Describe the morphology of the erythrocytes.
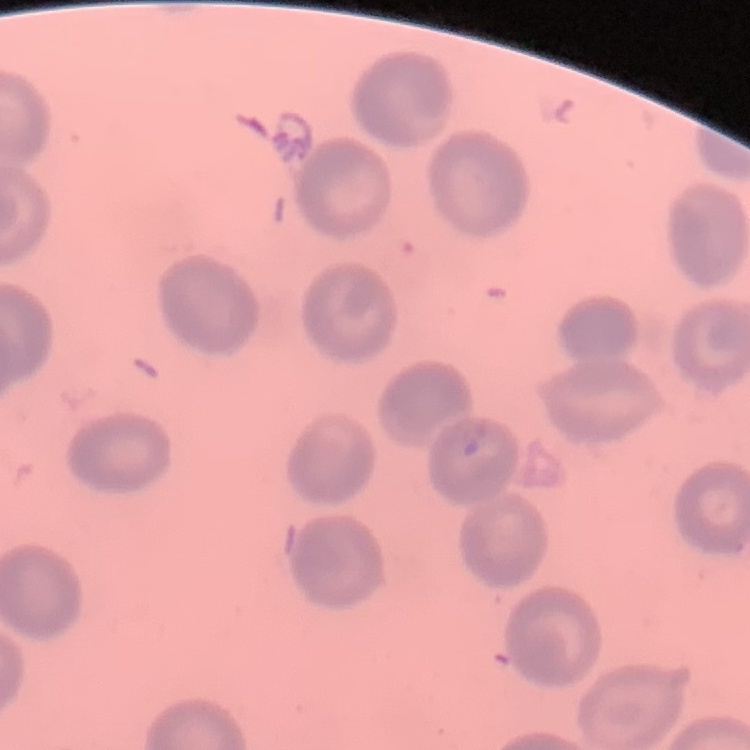
No rouleaux formation.

Square crop of a larger photomicrograph. Stained with either Field's or Giemsa. Thin peripheral smear.